Give the position of every Plasmodium parasite visible.
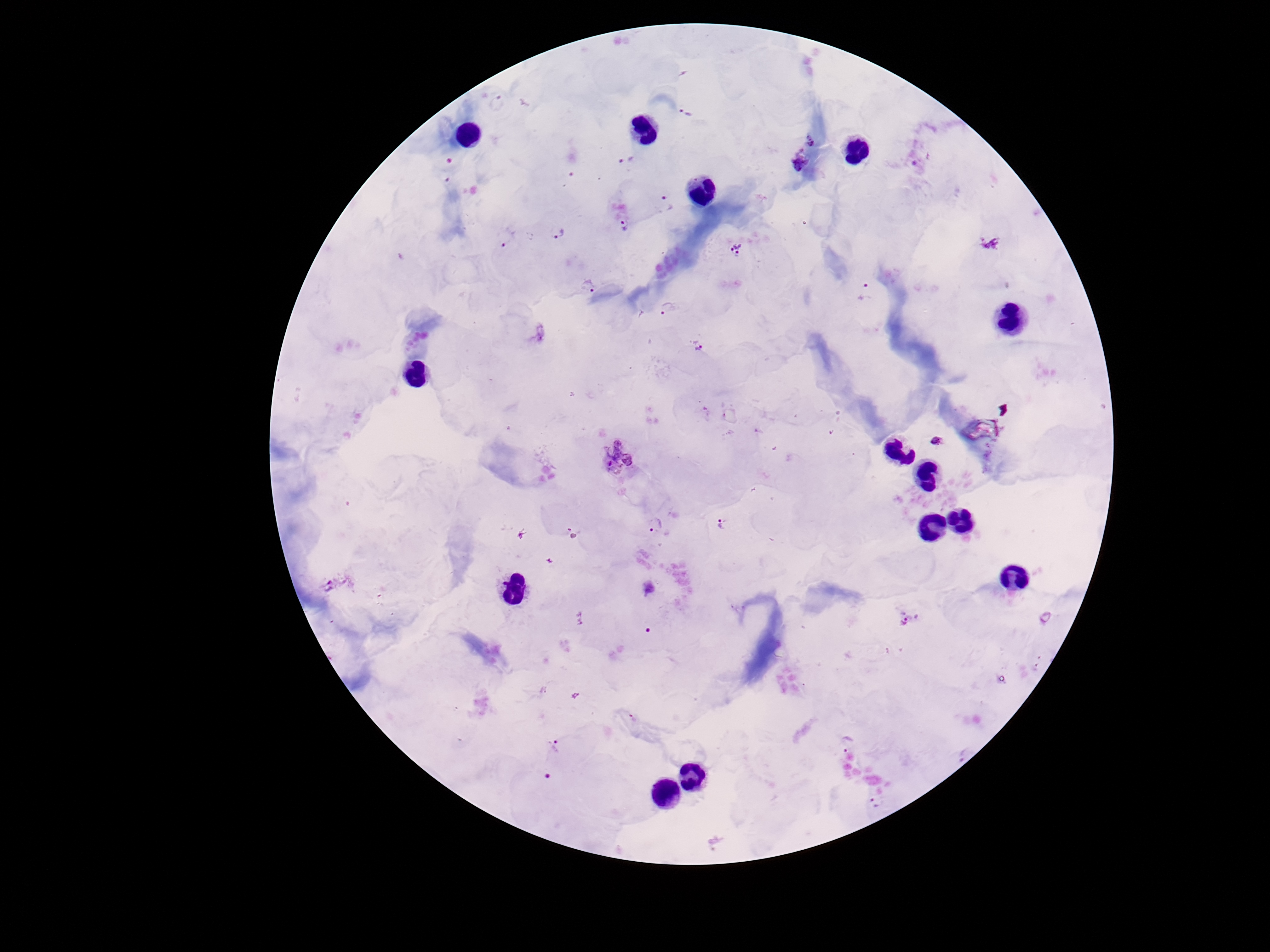

Approximate centers as (x, y) in pixels.
Plasmodium parasites: (498, 102), (686, 112), (811, 140), (625, 160), (799, 162), (624, 226), (557, 232), (505, 237), (990, 242), (735, 250), (586, 286), (864, 292), (666, 308), (698, 347), (935, 442), (617, 457), (655, 524), (720, 525), (327, 584), (907, 622), (553, 745), (874, 803).

Summary:
  - Stain: Giemsa
  - Capture: smartphone camera through the microscope eyepiece
  - Field of view: single
  - Patient malaria status: infected
  - Magnification: 100x
  - Preparation: thick peripheral-blood smear
  - Image size: 1270×952 pixels